Describe the morphology of the erythrocytes.
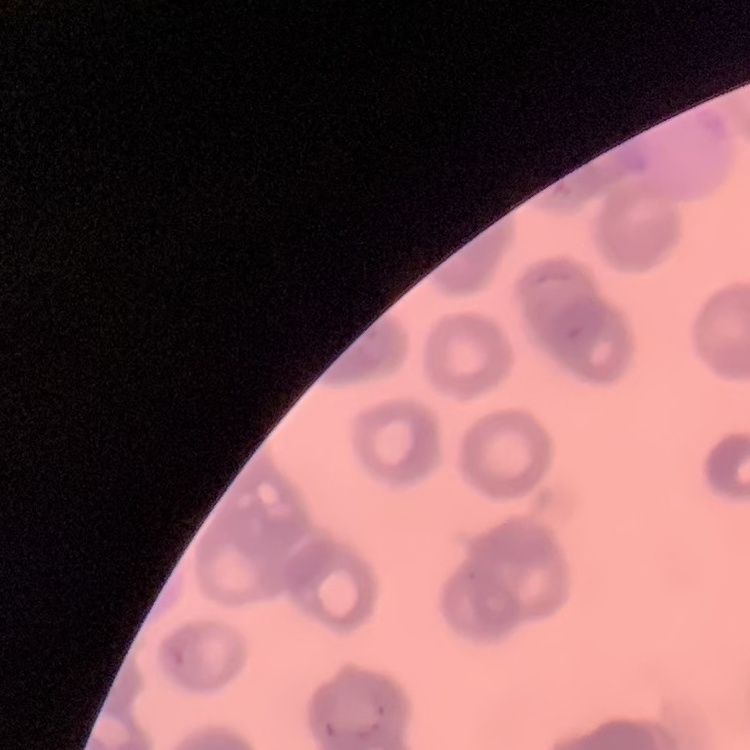
They show rouleaux formation.

Summary:
  - Preparation: thin blood smear
  - Stain: Field's or Giemsa
  - Image type: square crop of a larger photomicrograph